Assess this cell for malaria.
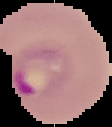

It is parasitized.

From a thin blood film. Segmented cell region on a black background. Image is 112×127 pixels.